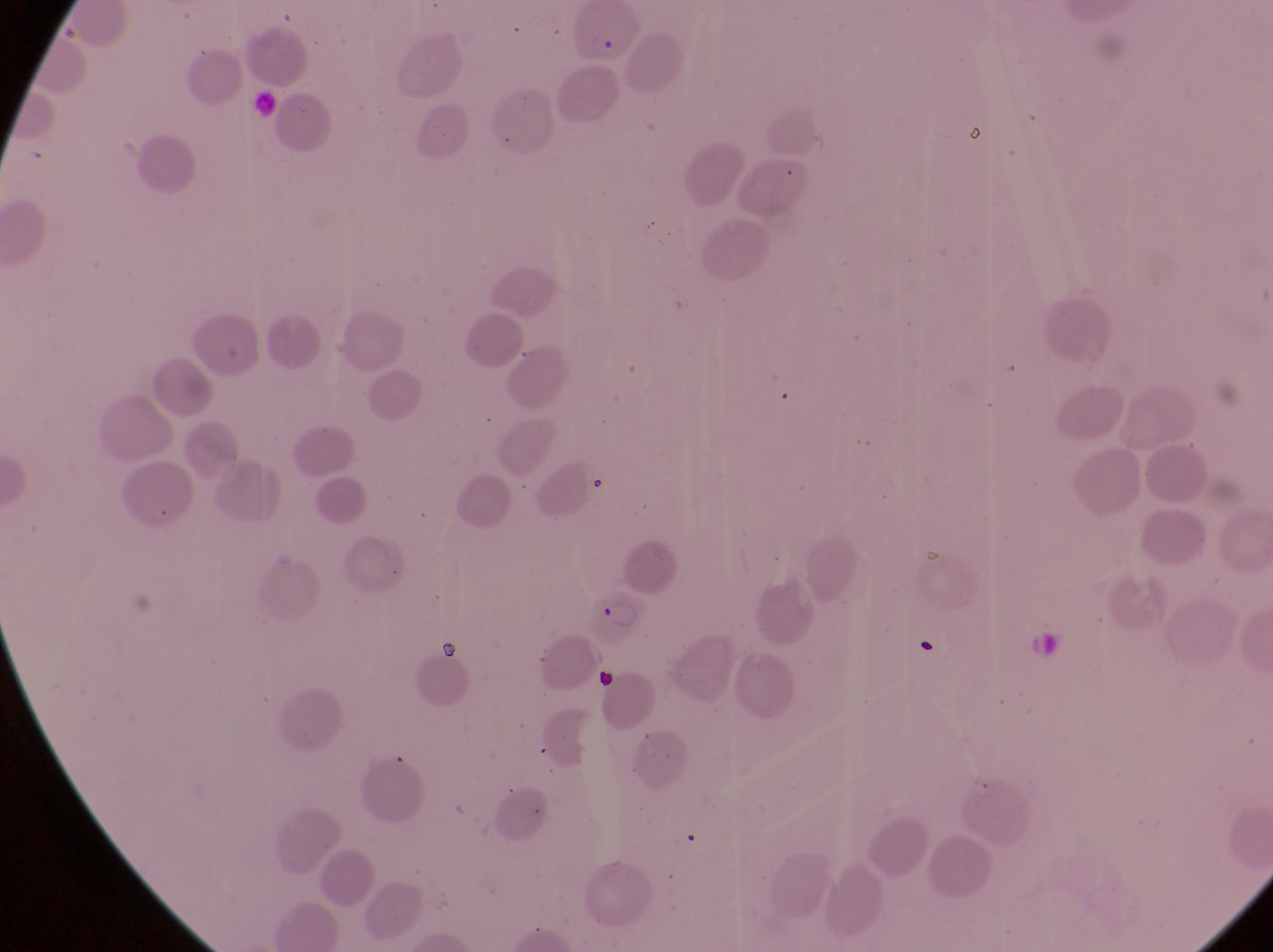

{
  "artifact_platelet_like_body_stain_precipitate_or_debris_locations": "approximate bounding boxes as {left, top, right, bottom} in pixels: {593, 664, 624, 692}",
  "preparation": "thin blood film",
  "capture": "smartphone photograph through the eyepiece of an Olympus CX-23 microscope",
  "magnification": "1000x",
  "field_of_view": "single",
  "image_size": "1273×952 pixels",
  "parasitised_red_blood_cell_locations": "approximate bounding boxes as {left, top, right, bottom} in pixels: {565, 8, 645, 68}, {587, 591, 639, 644}",
  "country": "Uganda"
}